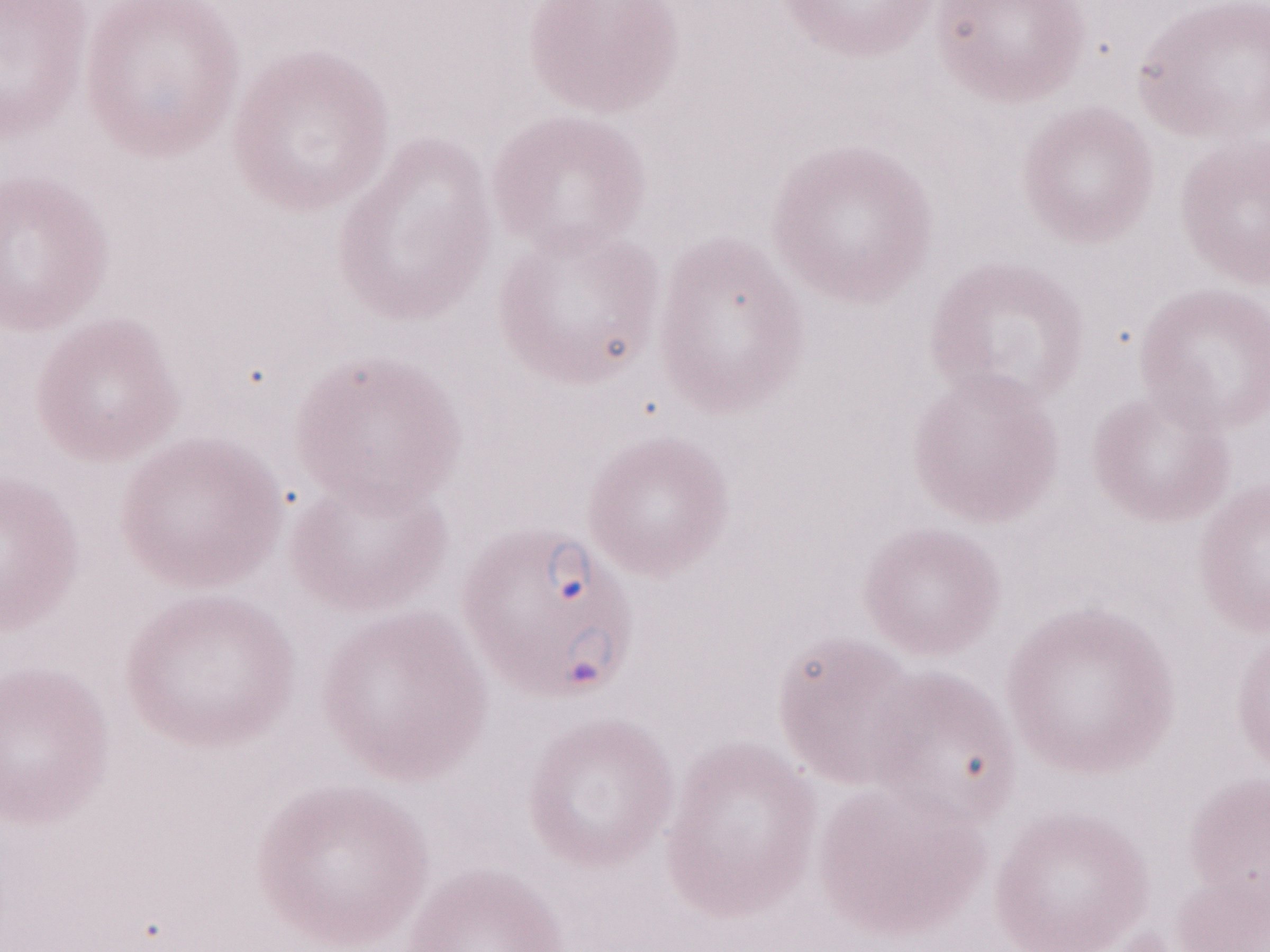 Olympus BX43 microscope and DP73 digital camera. Single field of view. Thin peripheral-blood smear. May-Grünwald-Giemsa-stained preparation. Patient diagnosis: malaria infection. Image is 1270×952 pixels. 1,000x magnification.